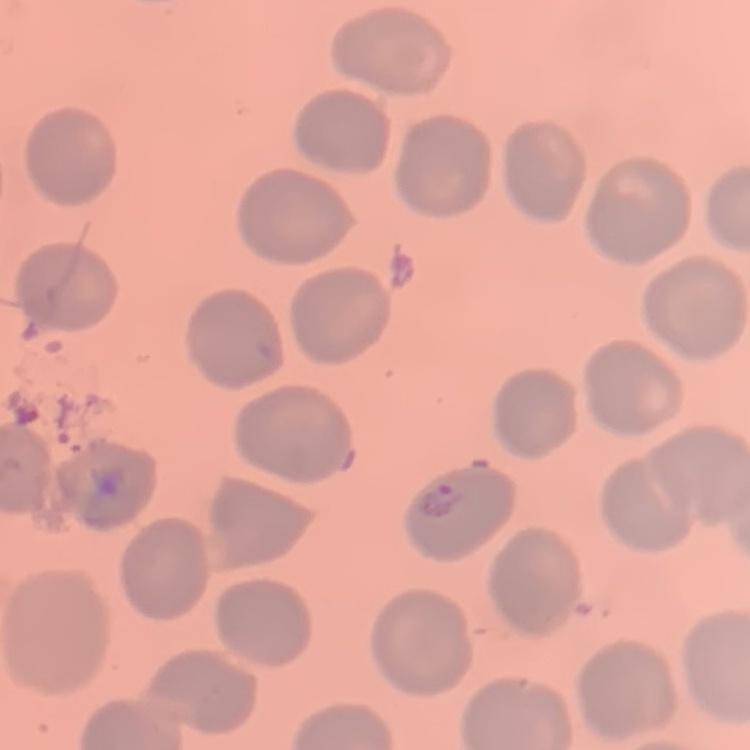
{
  "erythrocyte_morphology": "no rouleaux formation",
  "preparation": "thin blood smear",
  "stain": "Field's or Giemsa",
  "image_type": "square crop of a larger photomicrograph"
}